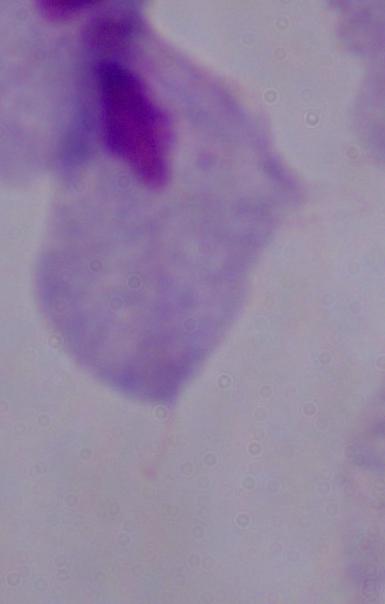

Micrograph. A trichomonad is shown. 1000x magnification.